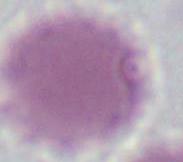

{
  "identification": "erythrocyte",
  "modality": "photomicrograph",
  "magnification": "1000x"
}